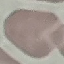
Summary:
  - Malaria status: uninfected
  - Preparation: thin blood smear
  - Capture: smartphone through the microscope eyepiece
  - Stain: Giemsa
  - Image type: automatically extracted cell patch, resized to 64 × 64 pixels